Assess this cell for malaria.
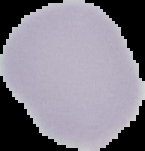

It is uninfected.

Summary:
  - Image size: 145×151 pixels
  - Image type: cell region segmented out of the field of view; surrounding area masked to black
  - Preparation: thin blood film